Assess this cell for malaria.
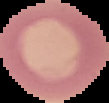

Uninfected.

Image is 109×103 pixels. From a thin blood film. The area outside the segmented cell region is set to black.